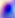

Summary:
  - Identification: Toxoplasma gondii
  - Modality: micrograph
  - Magnification: 400x